Locate every white blood cell.
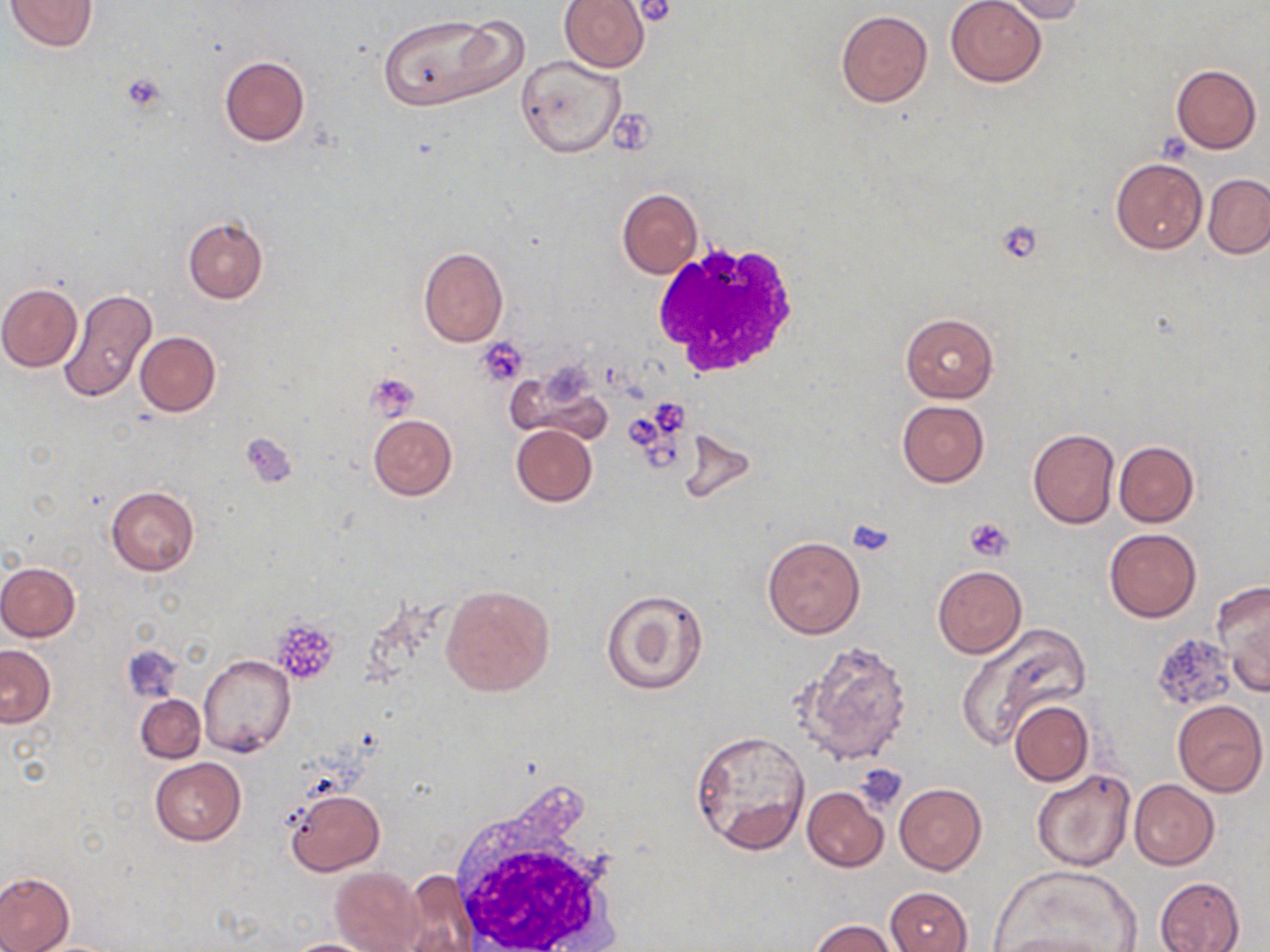

Approximate bounding boxes as [x1, y1, x2, y2] in pixels.
White blood cells: [649, 240, 802, 380], [447, 789, 624, 952].

Uninfected red blood cell locations: [6, 0, 99, 51], [560, 0, 650, 72], [944, 0, 1047, 86], [998, 0, 1085, 23], [835, 10, 933, 107], [376, 11, 523, 111], [516, 55, 626, 159], [219, 56, 310, 145], [1170, 64, 1262, 153], [1111, 157, 1207, 254], [1203, 174, 1270, 258], [616, 187, 703, 278], [182, 216, 269, 304], [418, 246, 508, 347], [0, 283, 83, 370], [58, 291, 157, 402], [900, 312, 998, 403], [135, 332, 221, 416], [506, 364, 607, 441], [896, 400, 988, 487], [367, 413, 457, 500], [511, 425, 597, 506], [1028, 429, 1120, 529], [678, 431, 757, 504], [1114, 440, 1198, 527], [106, 486, 200, 575], [1105, 528, 1201, 622], [763, 535, 865, 638], [0, 561, 79, 641], [932, 564, 1027, 659], [1215, 582, 1270, 695], [442, 584, 556, 697], [602, 589, 709, 695], [958, 622, 1088, 750], [795, 641, 913, 765], [122, 644, 183, 701], [0, 645, 57, 727], [199, 654, 295, 757], [136, 694, 204, 763], [1171, 699, 1266, 797], [1009, 700, 1093, 786], [690, 729, 811, 854], [150, 756, 246, 846], [1032, 768, 1135, 871], [1129, 779, 1219, 870], [895, 783, 986, 874], [802, 786, 888, 870], [286, 787, 385, 877], [995, 865, 1138, 950], [330, 866, 426, 952], [402, 870, 475, 949], [0, 872, 74, 952], [1154, 877, 1247, 951], [884, 886, 972, 952], [811, 918, 898, 952], [994, 930, 1118, 952], [281, 938, 381, 952]. Platelet locations: [634, 0, 676, 26], [121, 71, 168, 113], [611, 111, 657, 154], [994, 221, 1044, 263], [477, 338, 528, 385], [366, 373, 420, 421], [657, 402, 687, 440], [628, 415, 660, 450], [240, 432, 297, 489], [965, 517, 1013, 562], [848, 518, 895, 556], [270, 620, 339, 685], [854, 765, 908, 811]. Slide-level diagnosis: negative for blood parasites. Light microscopy. Captured at 1000x magnification. May-Grünwald-Giemsa stain. Thin blood smear. One field of a larger specimen. Image is 1270×952 pixels.